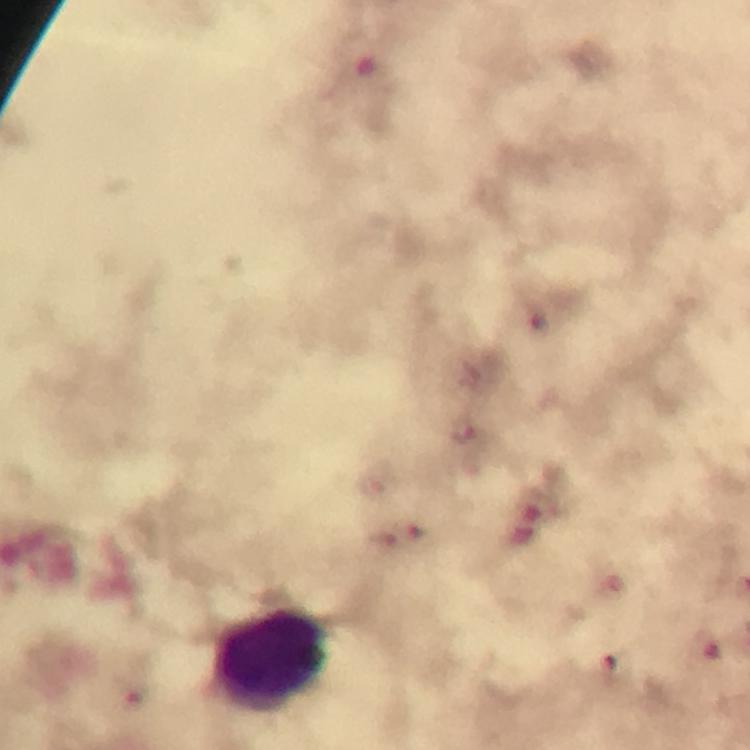
Approximate object centers, in pixels from the top-left corner. Leukocyte locations: (x=272, y=661). Plasmodium parasite locations: (x=464, y=431). At 100x magnification. From a diagnostic examination for malaria. Giemsa-stained preparation. Photographed with a smartphone mounted on the microscope. Immersion oil applied. A crop from one field of view. Thick blood film. Image is 750×750 pixels.